Report the malaria status of this cell.
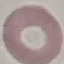

It is uninfected.

Acquired by smartphone through the microscope eyepiece. Thin blood film. Giemsa stain. Cell patch, automatically extracted from a larger field of view and resized to 64 × 64 pixels.